State which parasite is depicted.
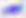
Toxoplasma gondii.

Summary:
  - Modality: photomicrograph
  - Magnification: 400x